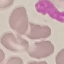 Malaria status: uninfected. Cell patch, automatically extracted from a larger field of view and resized to 64 × 64 pixels. Thin blood film. Photographed with a smartphone camera at the microscope eyepiece. Giemsa-stained preparation.